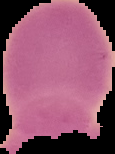

image size = 115×154 pixels
image type = cell region segmented out of the field of view; surrounding area masked to black
preparation = thin blood smear
result = negative for Plasmodium parasites